Describe the morphology of the erythrocytes.
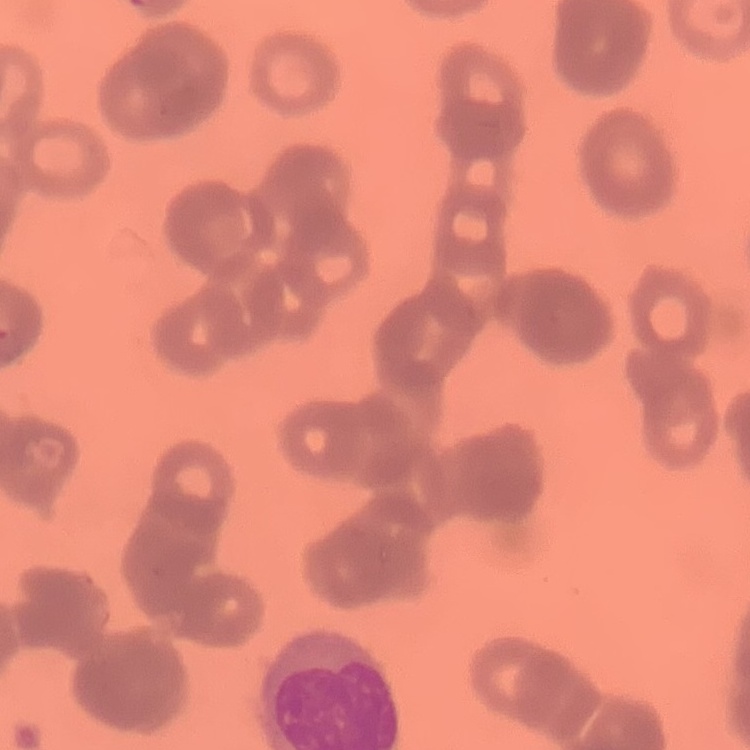
Rouleaux formation.

{
  "image_type": "one tile cut from a larger photomicrograph",
  "preparation": "thin peripheral smear",
  "stain": "Field's or Giemsa"
}